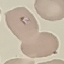
Result: malaria parasites identified. Acquired by smartphone through the microscope eyepiece. Thin blood film. Giemsa stain. Cell patch, automatically extracted from a larger field of view and resized to 64 × 64 pixels.